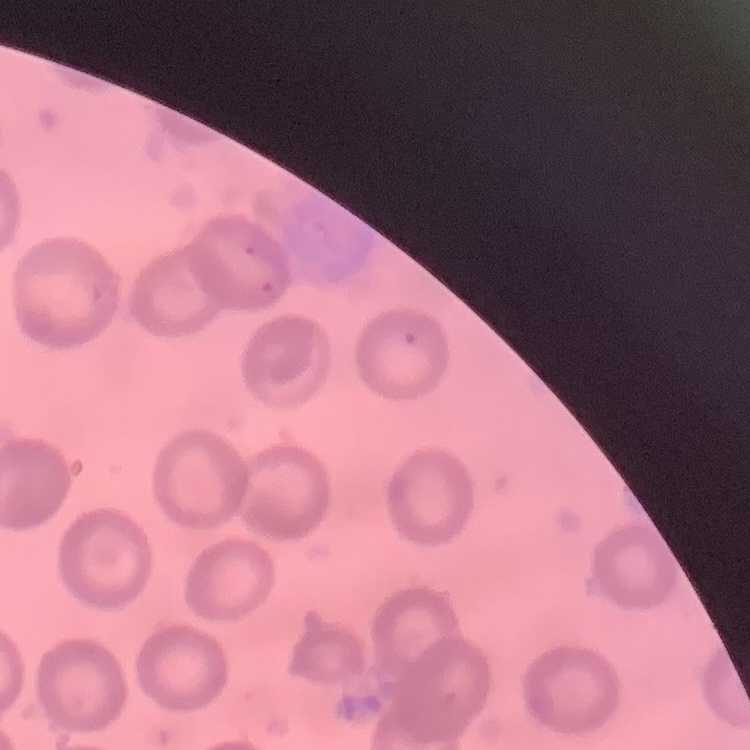
Summary:
  - Red blood cell morphology: no rouleaux formation
  - Image type: one tile cut from a larger photomicrograph
  - Preparation: thin blood smear
  - Stain: Field's or Giemsa